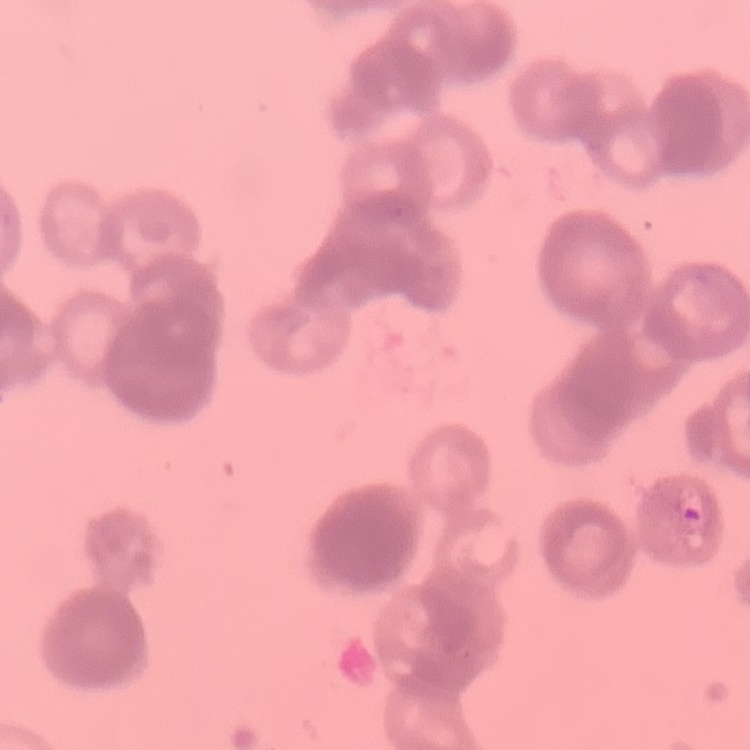
red blood cell morphology = rouleaux formation
preparation = thin blood smear
stain = Field's or Giemsa
image type = one tile cut from a larger photomicrograph